Locate every blood parasite and identify its species.
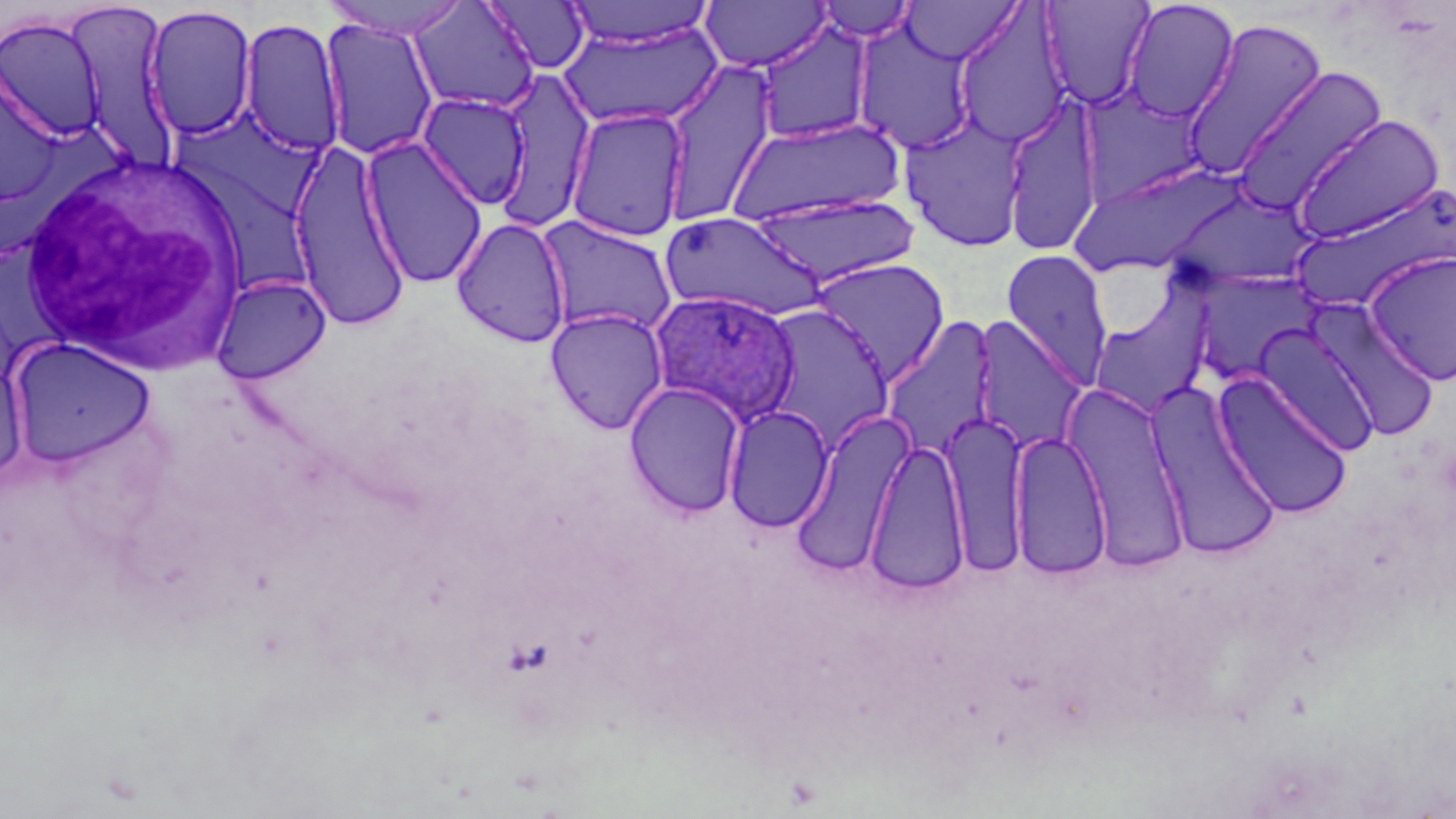
Approximate bounding boxes as [x1, y1, x2, y2] in pixels.
Plasmodium ovale-infected red blood cells: [648, 290, 800, 425].
No Plasmodium falciparum, Plasmodium malariae, Plasmodium vivax, Babesia divergens, or Trypanosoma brucei observed.

Summary:
  - Uninfected red blood cell locations: [322, 0, 473, 40], [900, 0, 1022, 64], [1039, 0, 1156, 111], [1121, 0, 1240, 123], [407, 1, 541, 114], [484, 1, 591, 74], [562, 1, 717, 48], [700, 1, 830, 72], [813, 1, 919, 42], [64, 2, 181, 168], [142, 5, 257, 141], [952, 6, 1074, 149], [1, 16, 106, 141], [238, 17, 346, 157], [1179, 17, 1329, 179], [320, 18, 439, 161], [852, 21, 979, 153], [559, 22, 722, 130], [754, 22, 875, 144], [661, 61, 778, 225], [1230, 66, 1390, 214], [0, 68, 64, 207], [492, 68, 596, 230], [416, 92, 532, 210], [1001, 97, 1103, 256], [564, 106, 690, 242], [897, 110, 1033, 254], [1291, 113, 1446, 244], [727, 115, 906, 229], [185, 118, 330, 215], [359, 135, 489, 288], [287, 138, 411, 332], [176, 155, 316, 294], [1069, 161, 1247, 278], [1290, 183, 1454, 313], [1161, 187, 1321, 289], [746, 193, 922, 288], [660, 211, 826, 322], [535, 215, 679, 338], [451, 216, 571, 348], [1001, 248, 1114, 389], [1363, 250, 1456, 386], [809, 257, 950, 384], [1185, 271, 1321, 387], [211, 274, 331, 383], [1089, 289, 1215, 420], [1306, 300, 1442, 442], [757, 303, 896, 450], [545, 307, 669, 434], [972, 316, 1090, 454], [880, 317, 999, 460], [1254, 325, 1381, 455], [7, 337, 157, 469], [0, 357, 28, 483], [1214, 372, 1353, 519], [624, 381, 746, 518], [1062, 383, 1191, 568], [1148, 384, 1283, 561], [723, 405, 834, 533], [789, 407, 916, 577], [938, 408, 1029, 577], [1008, 429, 1112, 580], [864, 439, 970, 594]
  - White blood cell locations: [19, 153, 252, 372]
  - Slide-level diagnosis: Plasmodium ovale
  - Modality: light microscopy
  - Preparation: thin blood smear
  - Stain: May-Grünwald-Giemsa
  - Image size: 1456×819 pixels
  - Field of view: one of a larger specimen
  - Magnification: 1000x